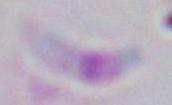

modality = micrograph
magnification = 1000x
identification = Toxoplasma gondii